Report the malaria status of this cell.
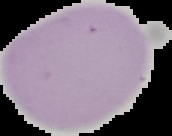
Uninfected.

{
  "preparation": "thin blood film",
  "image_type": "segmented cell region on a black background",
  "image_size": "172×136 pixels"
}